Locate every blood parasite and identify its species.
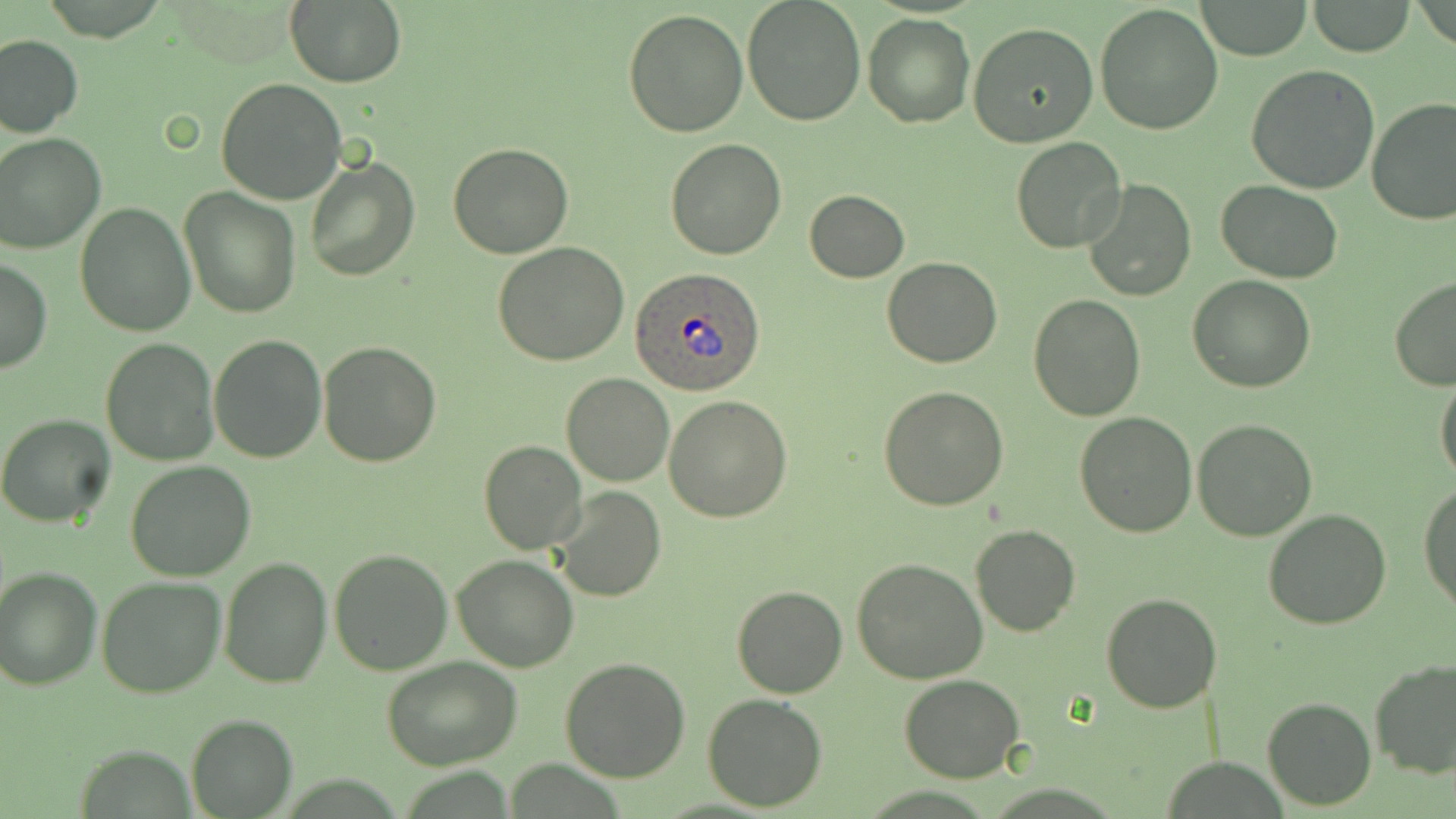

Approximate bounding boxes as (x1,y1)-(x2,y2) corner pairs in pixels.
Plasmodium ovale-infected red blood cells: (629,268)-(767,396).
No Plasmodium falciparum, Plasmodium malariae, Plasmodium vivax, Babesia divergens, or Trypanosoma brucei observed.

{
  "slide_level_diagnosis": "Plasmodium ovale",
  "magnification": "1000x",
  "image_size": "1456×819 pixels",
  "preparation": "thin blood film",
  "modality": "light microscopy",
  "field_of_view": "one of a larger specimen",
  "stain": "May-Grünwald-Giemsa",
  "uninfected_red_blood_cell_locations": "approximate bounding boxes as (x1,y1)-(x2,y2) corner pairs in pixels: (742,0)-(867,126), (1197,0)-(1312,59), (1309,0)-(1417,57), (286,2)-(406,87), (1094,3)-(1224,136), (622,9)-(749,137), (863,12)-(974,128), (968,22)-(1100,150), (0,35)-(83,138), (1246,66)-(1380,194), (215,78)-(349,205), (1366,98)-(1456,226), (1,133)-(104,254), (664,138)-(785,259), (1010,138)-(1126,255), (447,143)-(575,259), (303,156)-(419,282), (1083,179)-(1196,301), (1218,182)-(1344,284), (179,185)-(303,318), (804,189)-(910,282), (75,202)-(195,335), (493,242)-(628,368), (0,256)-(52,375), (882,256)-(1001,368), (1187,273)-(1315,393), (1389,277)-(1456,389), (1028,295)-(1145,422), (208,334)-(327,463), (101,337)-(218,466), (317,341)-(442,466), (1435,371)-(1456,484), (560,373)-(675,487), (877,386)-(1009,512), (662,395)-(792,523), (1076,413)-(1196,536), (1,414)-(118,528), (1192,418)-(1319,540), (478,438)-(587,554), (125,461)-(257,582), (1419,481)-(1456,613), (552,486)-(666,603), (1263,509)-(1392,629), (971,524)-(1081,637), (329,549)-(454,675), (451,555)-(579,673), (219,556)-(334,688), (852,558)-(987,683), (0,567)-(101,691), (95,575)-(227,699), (731,583)-(848,698), (1100,592)-(1221,713), (383,658)-(521,770), (560,658)-(691,782), (1369,658)-(1456,779), (899,674)-(1023,783), (701,693)-(829,811), (1261,695)-(1376,810), (186,714)-(297,818)"
}